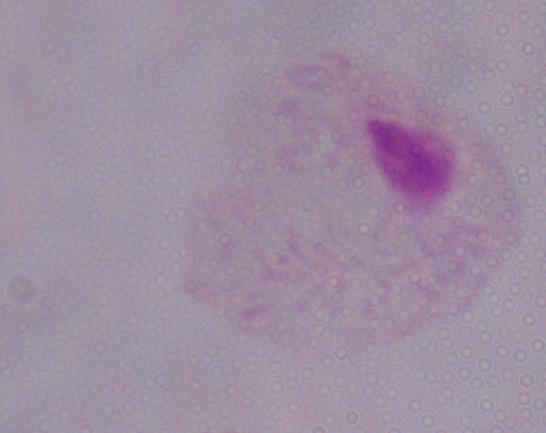

{
  "modality": "micrograph",
  "magnification": "1000x",
  "identification": "trichomonad"
}